Name the blood parasite species.
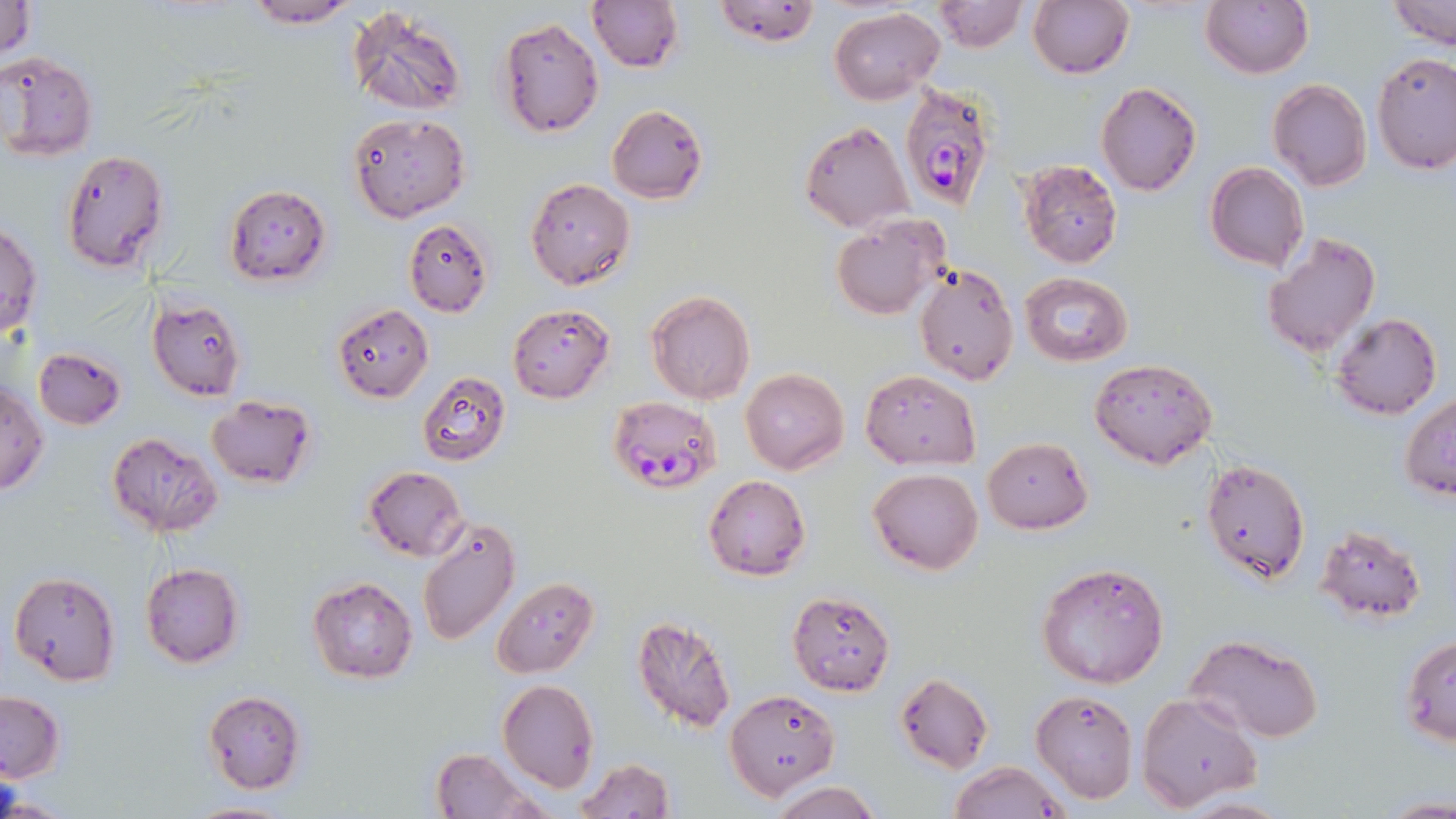

Plasmodium falciparum.

Approximate bounding boxes as [x1, y1, x2, y2] in pixels. Plasmodium falciparum-infected red blood cell locations: [899, 82, 1001, 214], [609, 397, 723, 496]. Uninfected red blood cell locations: [0, 0, 36, 58], [239, 0, 363, 29], [586, 0, 682, 72], [710, 0, 823, 47], [1026, 0, 1134, 80], [1200, 0, 1313, 79], [1388, 0, 1455, 48], [934, 1, 1025, 52], [347, 5, 468, 116], [828, 7, 944, 105], [497, 16, 605, 137], [0, 51, 98, 162], [1371, 51, 1456, 175], [1267, 78, 1371, 192], [1095, 82, 1202, 196], [607, 104, 708, 203], [348, 112, 469, 222], [801, 122, 916, 233], [60, 149, 170, 275], [1018, 159, 1122, 269], [1205, 162, 1309, 272], [526, 177, 634, 289], [224, 184, 331, 286], [829, 215, 948, 319], [404, 219, 493, 316], [0, 223, 42, 338], [1261, 233, 1381, 359], [915, 262, 1019, 387], [1019, 273, 1132, 366], [646, 290, 755, 405], [146, 295, 245, 402], [333, 303, 434, 402], [508, 304, 615, 402], [1331, 313, 1442, 420], [34, 346, 126, 429], [1089, 358, 1218, 469], [740, 367, 849, 475], [859, 369, 981, 469], [417, 371, 512, 466], [1, 381, 47, 495], [206, 395, 316, 489], [1402, 395, 1456, 501], [106, 431, 222, 536], [983, 437, 1092, 532], [1201, 457, 1311, 584], [363, 466, 469, 562], [868, 467, 983, 575], [702, 473, 812, 581], [416, 517, 520, 647], [1314, 522, 1427, 622], [139, 562, 244, 668], [1037, 562, 1169, 688], [9, 570, 120, 684], [493, 577, 598, 678], [308, 578, 418, 683], [787, 590, 895, 695], [631, 615, 737, 732], [1185, 634, 1324, 742], [1401, 636, 1456, 746], [894, 671, 993, 774], [497, 680, 599, 791], [725, 689, 839, 799], [1030, 689, 1138, 803], [0, 690, 63, 782], [203, 690, 307, 794], [1135, 693, 1261, 811], [430, 748, 539, 819], [573, 758, 675, 818], [948, 760, 1070, 819], [766, 781, 883, 818], [0, 790, 70, 817], [1378, 794, 1455, 818], [1175, 797, 1292, 818], [185, 799, 296, 818]. Light microscopy. Image is 1456×819 pixels. Thin blood smear. May-Grünwald-Giemsa stain. Single field of view. 1000x magnification.